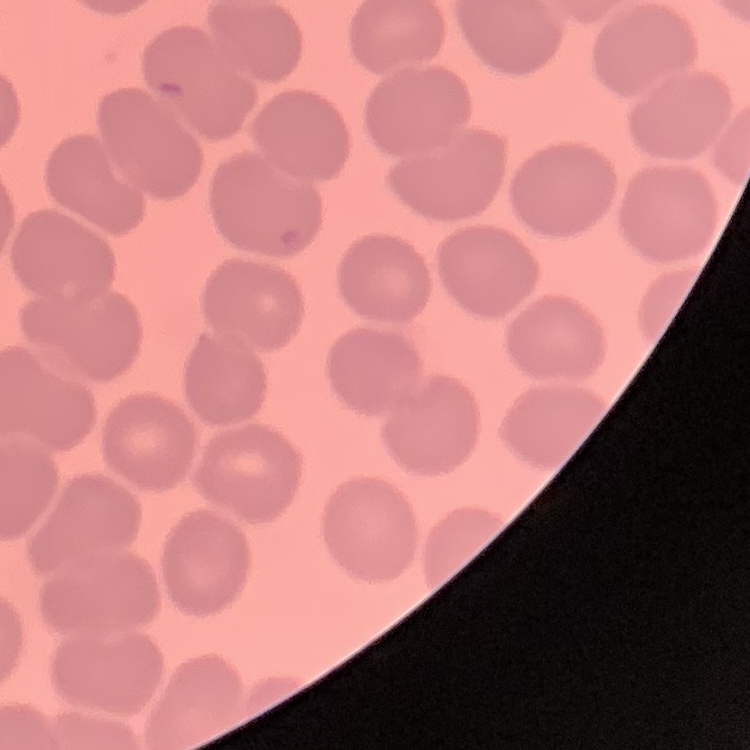
red blood cell morphology = no rouleaux formation
image type = square crop of a larger photomicrograph
preparation = thin blood film
stain = Field's or Giemsa